Classify this cell by malaria status.
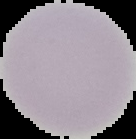

It is uninfected.

Image is 136×139 pixels. Segmented cell region on a black background. From a thin blood smear.